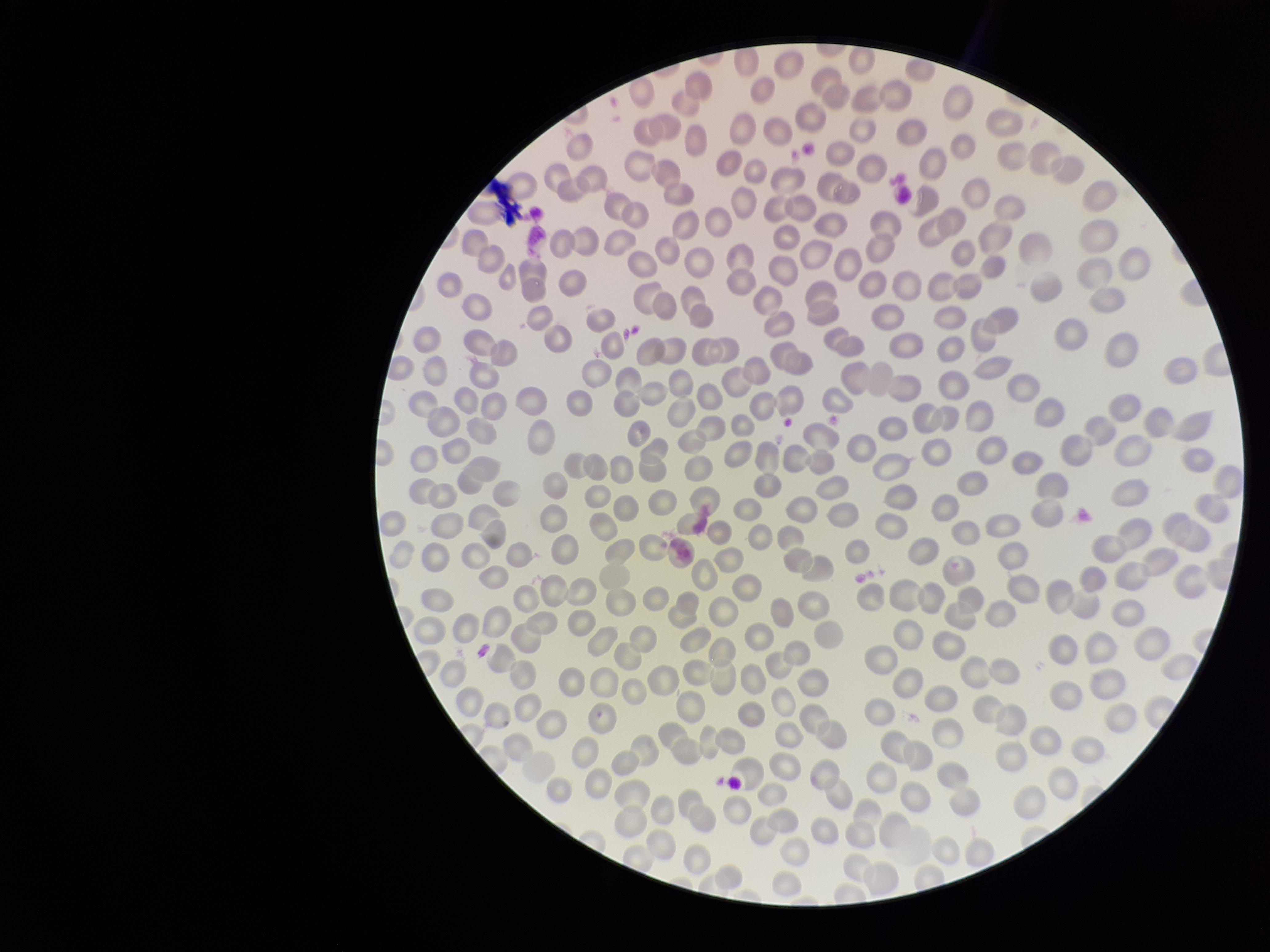
{
  "capture": "smartphone photograph through the microscope eyepiece",
  "parasitized_red_blood_cell_count": 0,
  "image_size": "1270×952 pixels",
  "stain": "Giemsa",
  "red_blood_cell_count": 296,
  "patient_malaria_status": "negative",
  "field_of_view": "single",
  "preparation": "thin blood smear",
  "parasitized_red_blood_cells": "none detected"
}